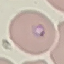
malaria status = parasitized
image type = cell patch, automatically extracted from a larger field of view and resized to 64 × 64 pixels
preparation = thin smear
capture = smartphone through the microscope eyepiece
stain = Giemsa